Locate every malaria parasite and every leukocyte.
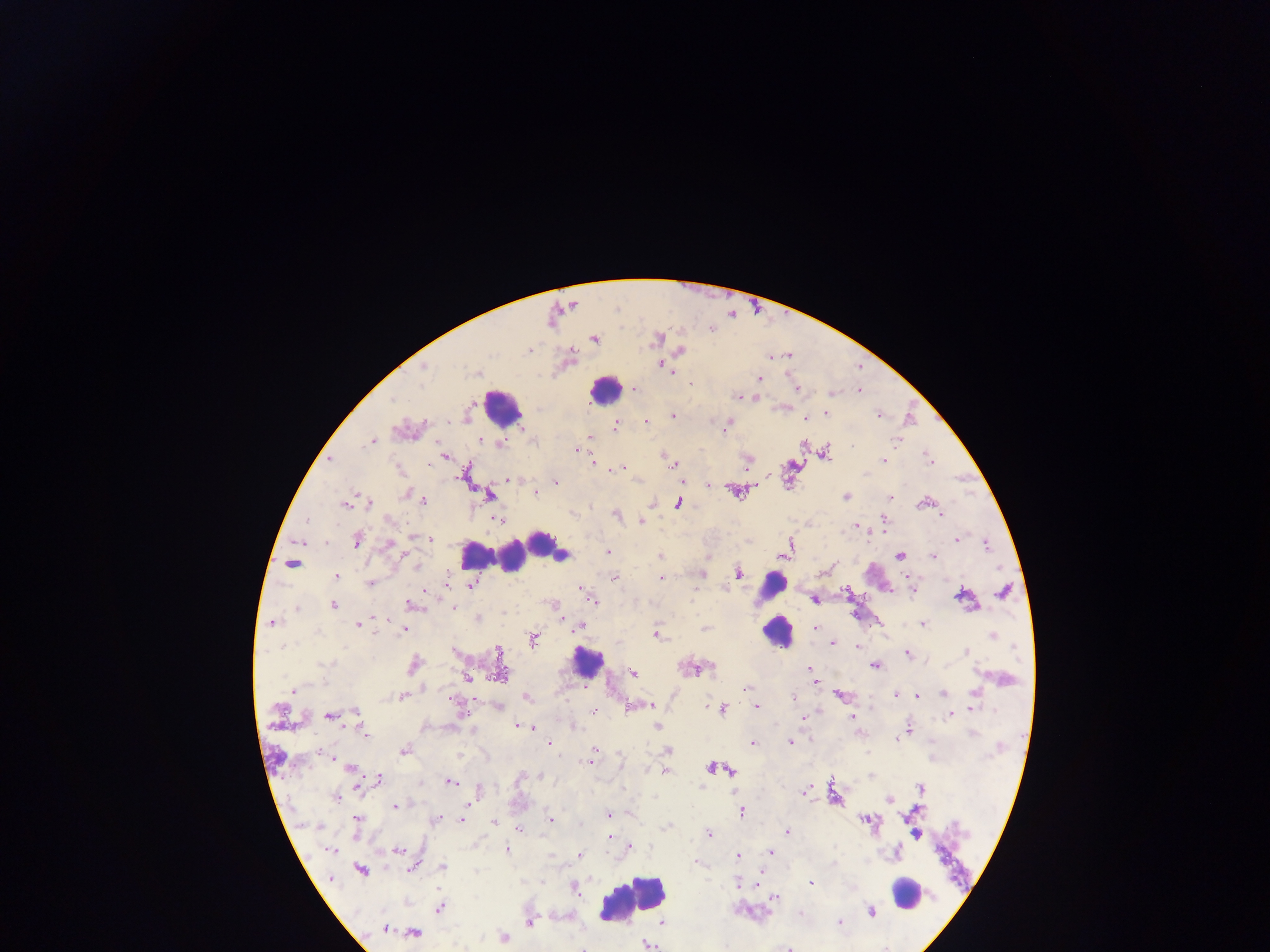

Approximate centers as [x, y] in pixels.
Malaria parasites: [616, 307], [658, 337], [595, 339], [679, 351], [661, 363], [668, 368], [425, 369], [672, 371], [758, 378], [424, 383], [690, 383], [858, 392], [831, 394], [740, 396], [752, 398], [395, 401], [827, 413], [877, 415], [673, 417], [805, 418], [728, 422], [646, 424], [616, 427], [726, 430], [479, 440], [370, 441], [895, 441], [483, 442], [829, 445], [501, 446], [576, 449], [827, 452], [830, 455], [446, 456], [663, 456], [883, 460], [929, 460], [670, 461], [329, 462], [592, 462], [748, 463], [431, 465], [673, 465], [790, 465], [621, 467], [617, 469], [612, 471], [863, 473], [508, 478], [683, 480], [557, 481], [731, 490], [535, 493], [406, 494], [489, 496], [846, 496], [892, 497], [424, 501], [369, 502], [653, 502], [678, 502], [923, 503], [344, 504], [916, 504], [938, 513], [617, 514], [940, 515], [498, 519], [885, 520], [641, 521], [854, 525], [411, 537], [867, 539], [956, 539], [356, 540], [432, 540], [301, 541], [388, 543], [988, 545], [789, 547], [607, 550], [563, 555], [785, 555], [660, 556], [900, 557], [933, 558], [292, 564], [999, 567], [739, 573], [702, 575], [614, 576], [336, 577], [660, 577], [369, 582], [448, 582], [471, 585], [725, 587], [847, 590], [913, 591], [1004, 591], [427, 593], [957, 596], [812, 597], [961, 597], [593, 599], [297, 606], [333, 606], [412, 606], [454, 607], [557, 608], [273, 624], [924, 624], [357, 625], [579, 625], [814, 627], [704, 628], [404, 630], [993, 634], [656, 635], [886, 636], [532, 641], [832, 644], [855, 647], [283, 649], [497, 652], [908, 653], [966, 653], [415, 664], [873, 665], [808, 668], [633, 673], [498, 674], [468, 678], [816, 685], [746, 687], [293, 692], [894, 694], [942, 694], [972, 694], [401, 695], [838, 695], [916, 695], [793, 696], [526, 698], [651, 706], [757, 708], [723, 709], [592, 710], [972, 710], [354, 712], [947, 715], [329, 717], [851, 717], [803, 718], [517, 726], [527, 726], [534, 726], [908, 727], [363, 730], [366, 734], [550, 742], [752, 742], [789, 742], [897, 742], [593, 749], [403, 751], [668, 751], [283, 761], [588, 764], [352, 767], [711, 767], [731, 771], [665, 772], [870, 774], [544, 775], [381, 778], [451, 782], [919, 787], [702, 789], [356, 790], [805, 792], [335, 798], [836, 800], [890, 801], [473, 803], [396, 806], [917, 809], [741, 812], [609, 813], [357, 818], [437, 819], [549, 820], [862, 820], [906, 820], [463, 821], [494, 822], [872, 822], [667, 825], [321, 828], [517, 828], [787, 831], [707, 834], [917, 836], [609, 837], [912, 838], [632, 846], [506, 850], [332, 851], [398, 851], [770, 851], [579, 853], [900, 853], [768, 854], [736, 856], [692, 860], [443, 866], [407, 868], [477, 870], [360, 871], [737, 883], [813, 884], [754, 887], [574, 889], [928, 895], [774, 899], [440, 908], [872, 911], [528, 922], [838, 923], [524, 926], [385, 930], [416, 932], [503, 938], [648, 944].
Leukocytes: [602, 393], [498, 404], [543, 545], [472, 555], [511, 563], [769, 586], [775, 637], [587, 662], [904, 894], [633, 896].

Thick blood film. Image is 1270×952 pixels. Single field of view. Mobile-phone photograph taken through the microscope. Sample from Ghana.